Report the malaria status of this cell.
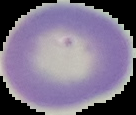
It is uninfected.

Cell region segmented out of the field of view; the surrounding area is masked to black. From a thin blood smear. Image is 136×115 pixels.